Describe the morphology of the erythrocytes.
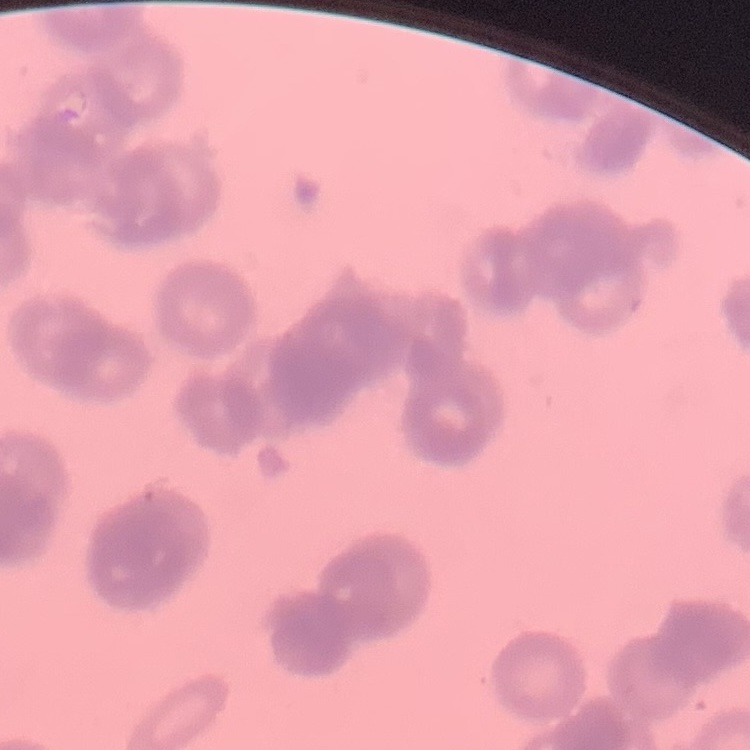

They show rouleaux formation.

preparation: thin blood film
stain: Field's or Giemsa
image_type: one tile cut from a larger photomicrograph